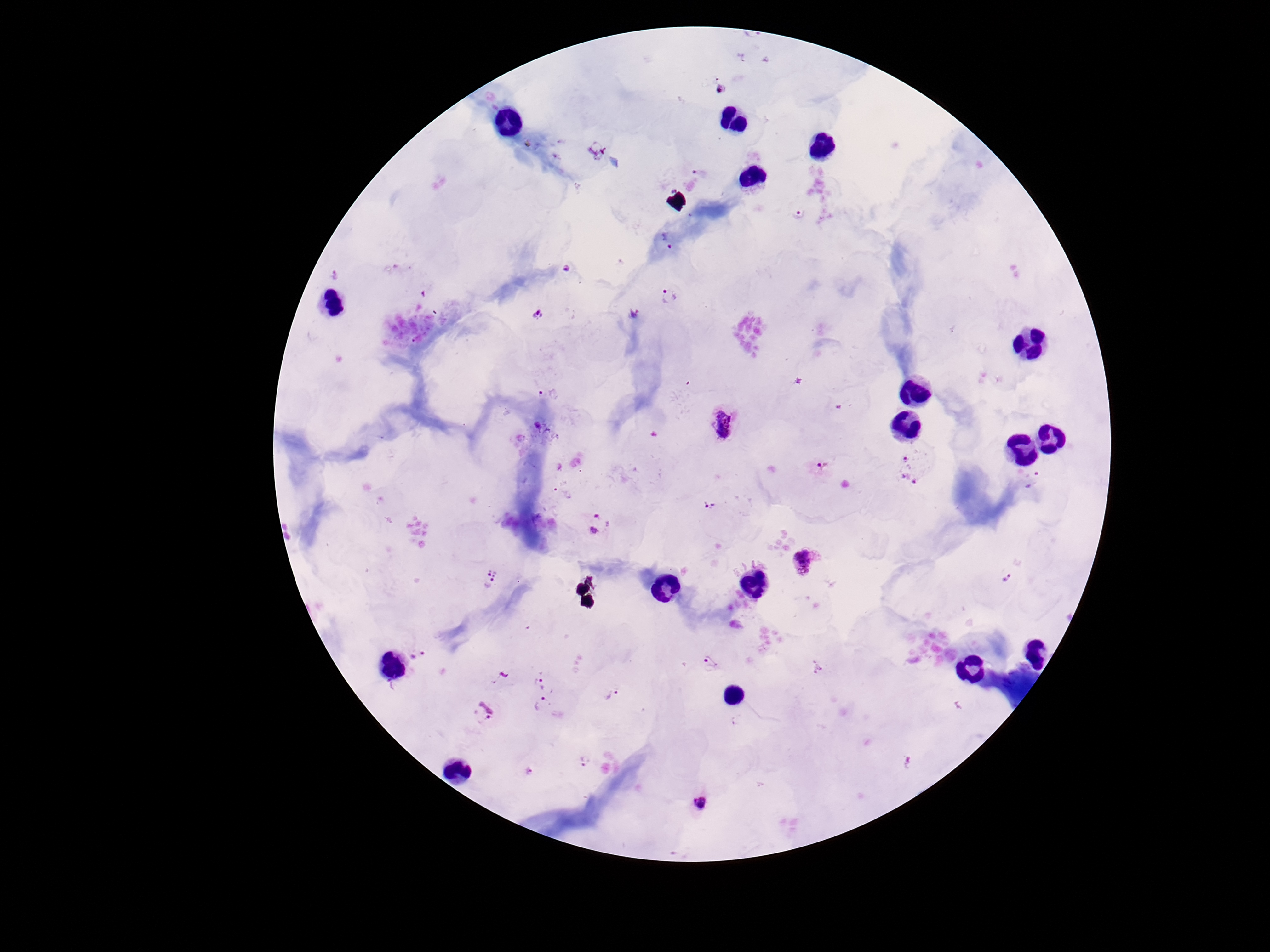 Approximate centers as (x, y) in pixels. Plasmodium parasite locations: (701, 171), (797, 213), (665, 241), (568, 269), (334, 276), (669, 297), (635, 312), (536, 315), (724, 425), (822, 465), (915, 466), (1036, 483), (564, 492), (708, 506), (598, 524), (803, 563), (490, 578), (1007, 579), (418, 654), (709, 665), (541, 683), (610, 694), (542, 706), (483, 712), (586, 759), (529, 773), (700, 804). 100x magnification. Patient malaria status: positive. Thick blood film. One field from this slide. Image is 1270×952 pixels. Giemsa stain. Smartphone photograph taken through the microscope eyepiece.